Classify this cell by malaria status.
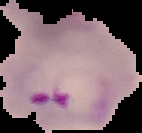

Parasitized.

Summary:
  - Image type: segmented cell region on a black background
  - Preparation: thin blood film
  - Image size: 142×133 pixels